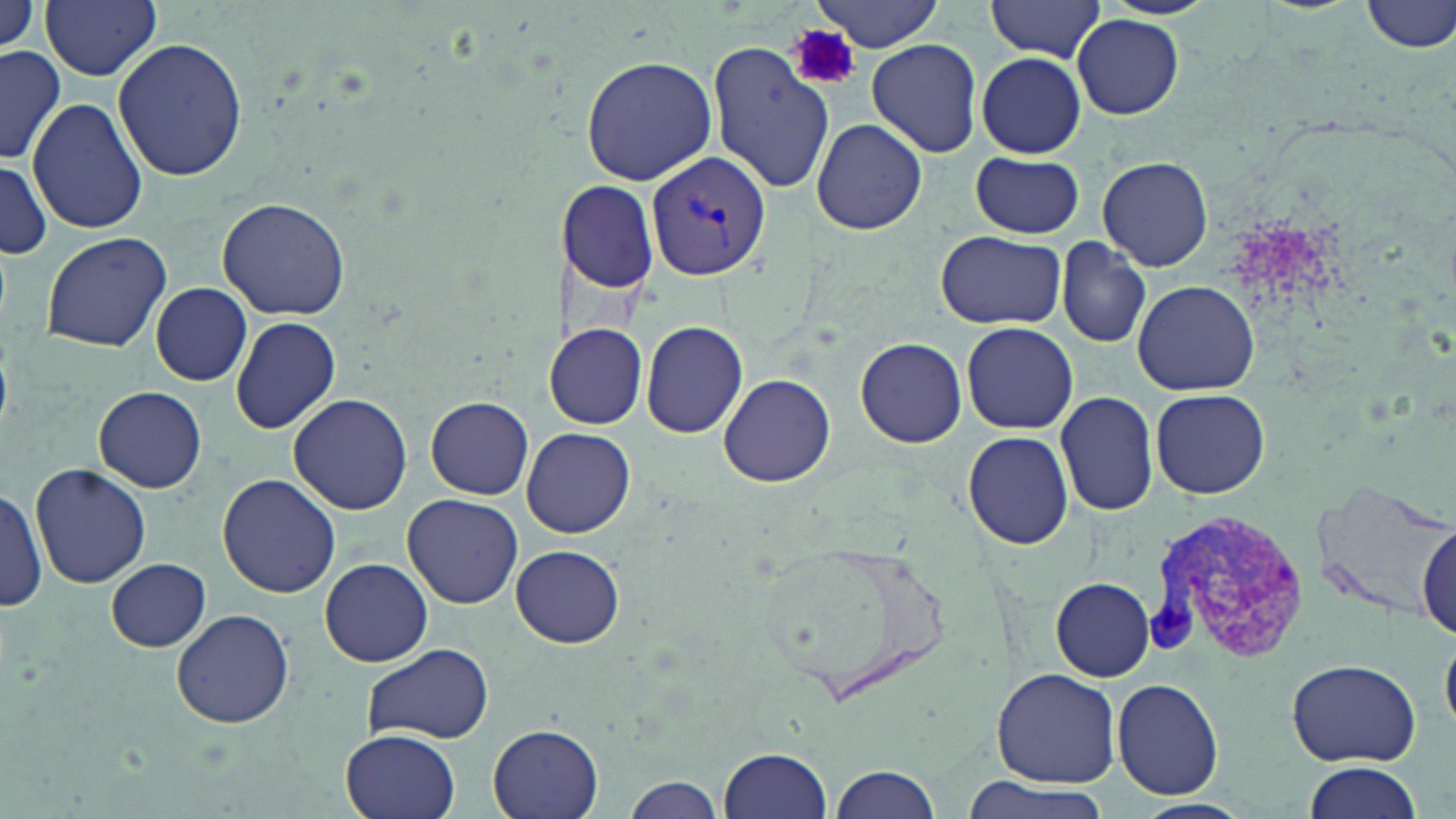

slide-level diagnosis = Plasmodium vivax
uninfected red blood cell locations = approximate bounding boxes as [x1, y1, x2, y2] in pixels: [0, 0, 43, 55], [40, 0, 163, 80], [985, 0, 1107, 62], [1362, 0, 1456, 54], [815, 1, 945, 51], [59, 10, 209, 125], [1073, 15, 1183, 119], [110, 37, 249, 183], [865, 38, 982, 157], [707, 40, 834, 196], [0, 45, 65, 165], [975, 52, 1087, 158], [581, 55, 717, 185], [27, 98, 147, 234], [812, 118, 926, 236], [969, 152, 1086, 238], [1098, 155, 1212, 274], [0, 160, 49, 258], [558, 179, 660, 295], [216, 196, 351, 320], [40, 230, 172, 353], [936, 230, 1066, 329], [1055, 237, 1153, 350], [1132, 280, 1259, 395], [152, 283, 251, 386], [230, 316, 340, 435], [640, 319, 749, 438], [961, 321, 1078, 434], [546, 323, 647, 429], [857, 337, 967, 449], [719, 372, 837, 488], [94, 385, 207, 493], [1150, 389, 1271, 497], [1055, 390, 1159, 517], [288, 394, 412, 514], [425, 395, 534, 499], [521, 427, 635, 538], [960, 431, 1075, 551], [30, 462, 153, 589], [218, 473, 340, 598], [1310, 478, 1455, 620], [0, 483, 46, 613], [403, 493, 524, 608], [1416, 522, 1454, 643], [759, 536, 956, 699], [512, 544, 623, 647], [106, 557, 210, 650], [320, 558, 433, 667], [1050, 576, 1156, 681], [170, 607, 295, 729], [1441, 631, 1455, 738], [361, 643, 493, 745], [1286, 658, 1422, 767], [993, 668, 1120, 788], [1111, 677, 1225, 799], [489, 726, 603, 819], [341, 730, 459, 819], [719, 746, 832, 818], [1300, 762, 1424, 819], [829, 766, 941, 818], [953, 775, 1115, 819], [622, 776, 726, 818], [1133, 800, 1253, 819]
magnification = 1000x
platelet locations = approximate bounding boxes as [x1, y1, x2, y2] in pixels: [788, 24, 860, 92]
preparation = thin blood film
field of view = single
image size = 1456×819 pixels
stain = May-Grünwald-Giemsa
Plasmodium vivax-infected red blood cell locations = approximate bounding boxes as [x1, y1, x2, y2] in pixels: [645, 149, 772, 282], [1148, 510, 1311, 661]
modality = optical microscopy